Describe the morphology of the erythrocytes.
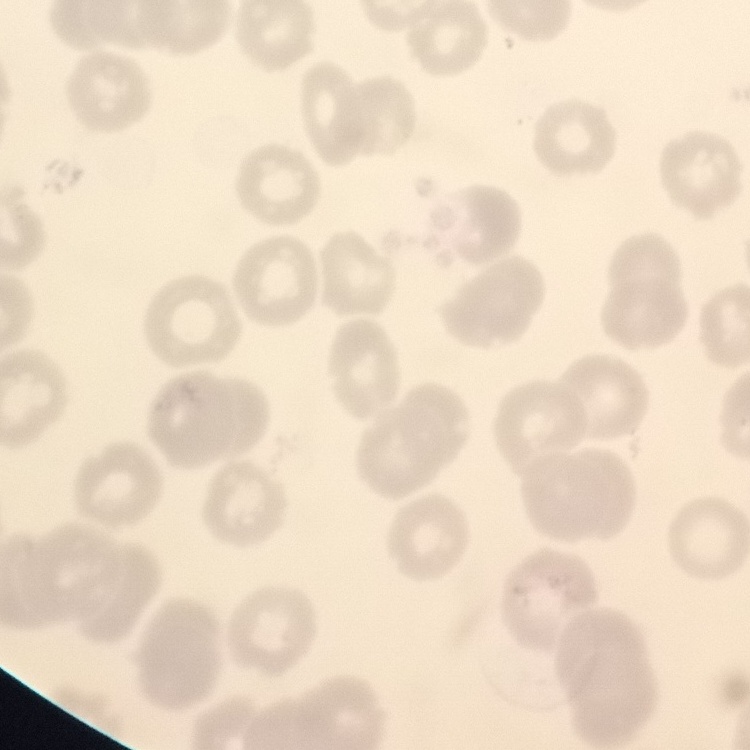
They show no rouleaux formation.

Summary:
  - Image type: square crop of a larger photomicrograph
  - Preparation: thin blood smear
  - Stain: Field's or Giemsa